Classify this cell by malaria status.
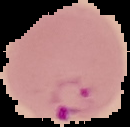
It is parasitized.

Summary:
  - Image size: 130×127 pixels
  - Preparation: thin blood smear
  - Image type: segmented cell region on a black background